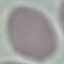
malaria status = uninfected
capture = smartphone camera at the microscope eyepiece
image type = cell patch, automatically extracted from a larger field of view and resized to 64 × 64 pixels
stain = Giemsa
preparation = thin blood smear